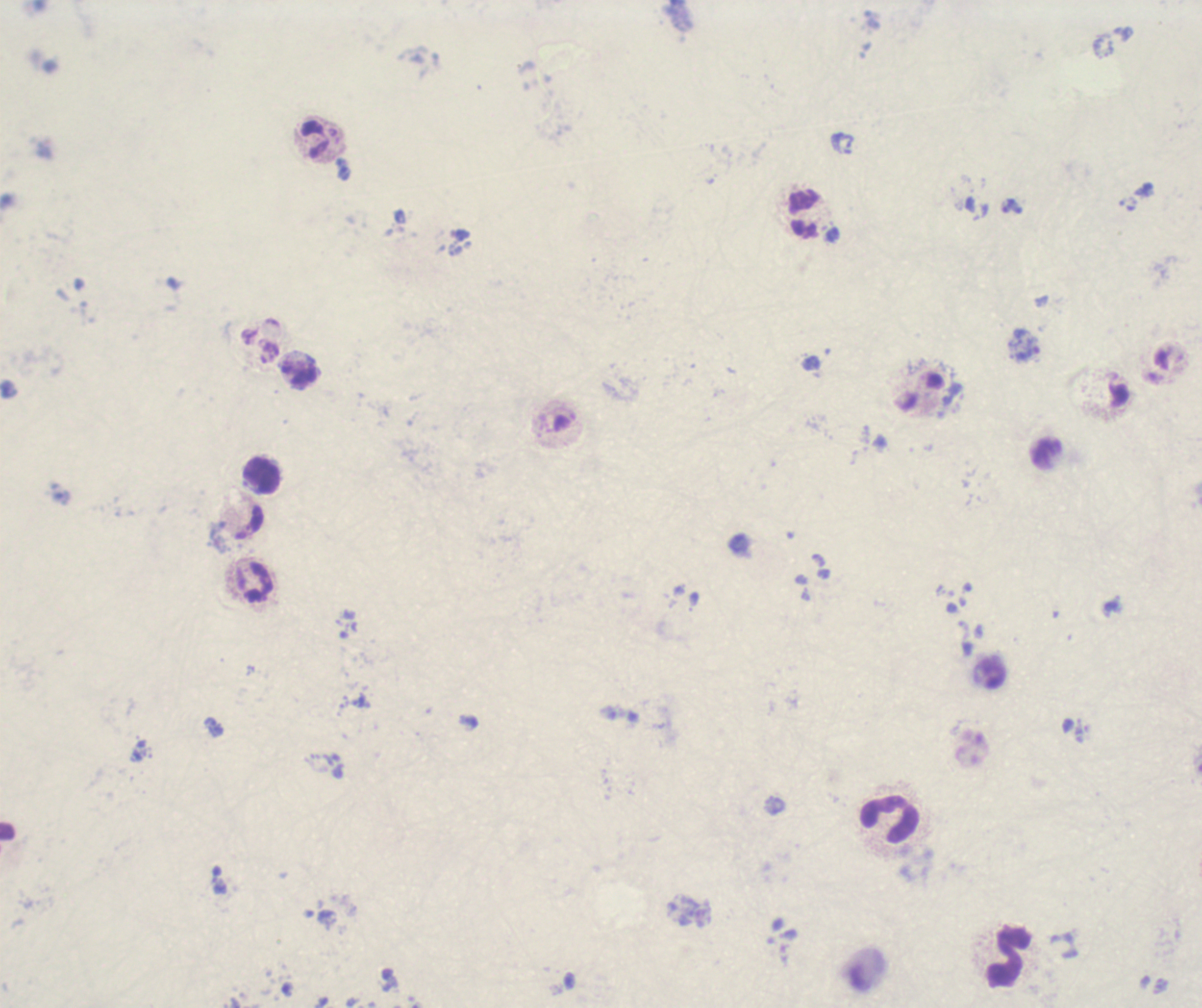
preparation: thick blood smear
background_quality: unsatisfactory
trophozoite_locations: 'approximate centers as [x, y] in pixels: [1024, 344]'
magnification: 100x
field_of_view: single
stain: Romanowsky
context: previously used in an actual diagnosis
image_size: 1202×1008 pixels
result: Plasmodium parasites detected
leukocyte_locations: 'approximate centers as [x, y] in pixels: [314, 139], [803, 214], [299, 375], [263, 475], [254, 582], [889, 819], [1010, 957]'